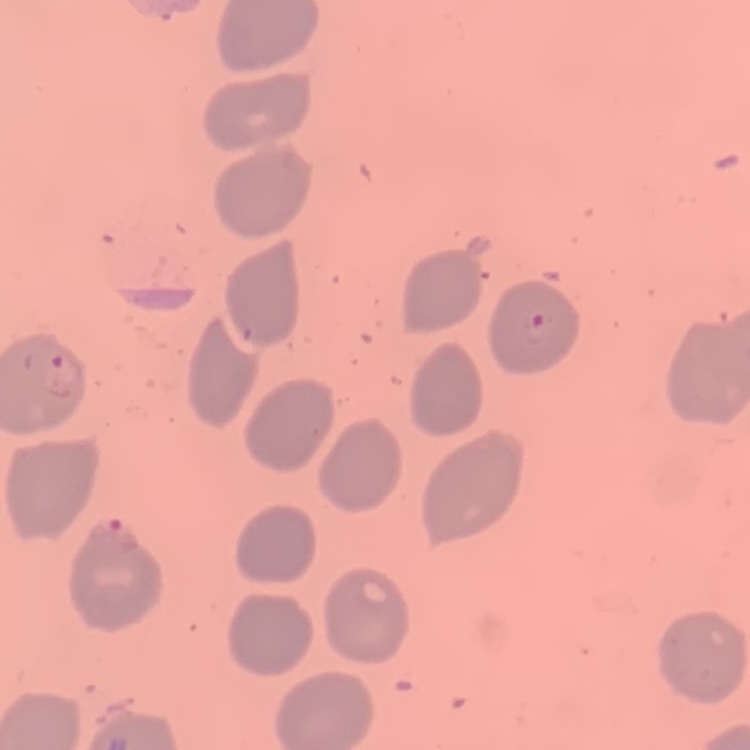 The erythrocytes show no rouleaux formation. Field's or Giemsa stain. One tile cut from a larger photomicrograph. Thin blood film.